State the blood parasite species.
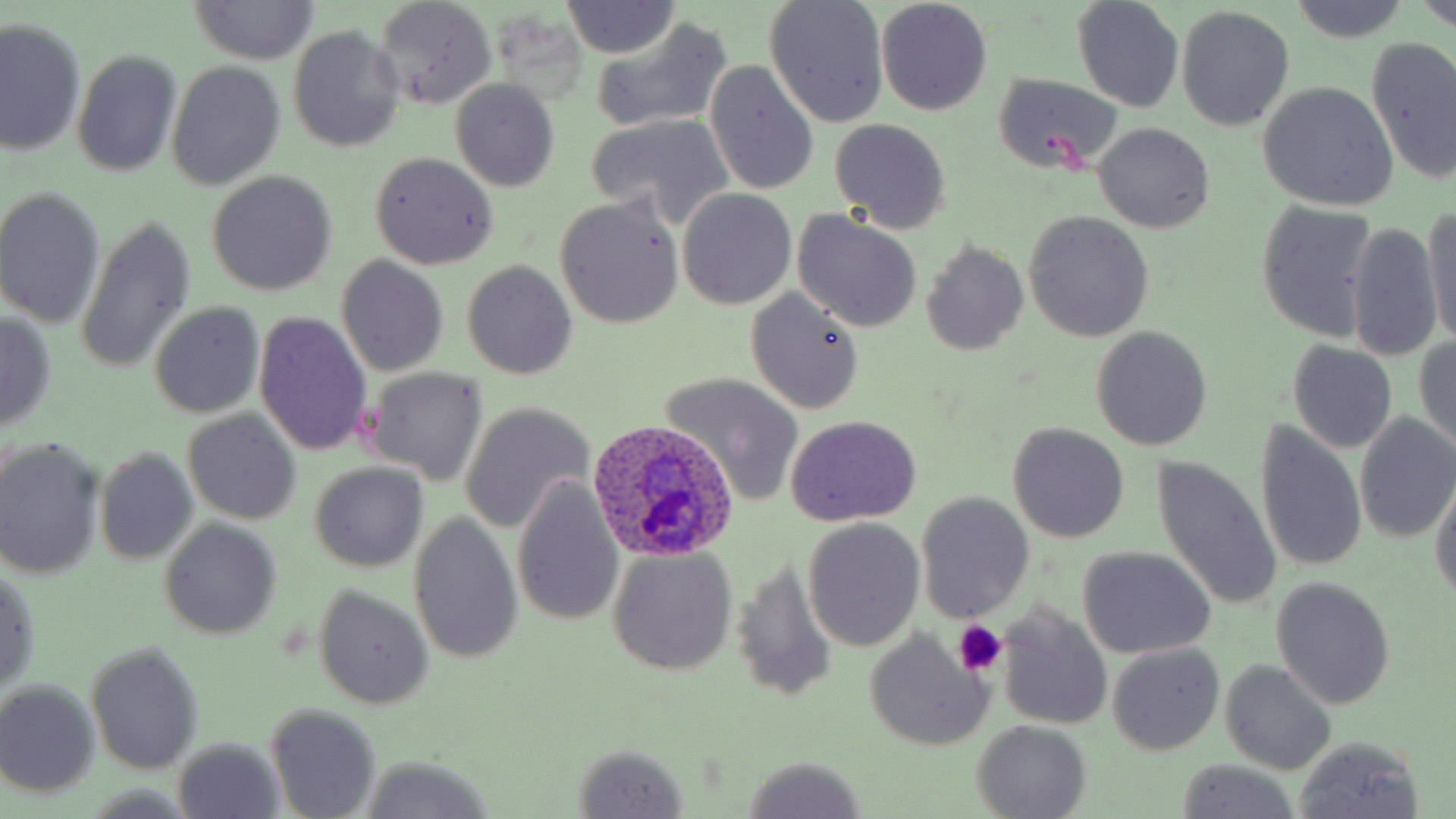
Plasmodium ovale.

Summary:
  - Coordinate format: approximate bounding boxes as (x1, y1, x2, y2) in pixels
  - Platelet locations: (951, 622, 1006, 676)
  - Uninfected red blood cell locations: (192, 0, 315, 65), (372, 0, 498, 110), (1289, 0, 1408, 42), (1420, 0, 1456, 30), (764, 1, 888, 127), (565, 2, 677, 58), (876, 2, 992, 115), (1073, 2, 1183, 113), (1177, 7, 1293, 131), (1, 18, 85, 158), (589, 18, 733, 135), (288, 25, 406, 153), (1365, 36, 1456, 187), (72, 50, 182, 177), (705, 60, 819, 196), (167, 62, 284, 188), (993, 74, 1120, 175), (450, 79, 559, 192), (1257, 82, 1397, 210), (585, 113, 735, 230), (830, 118, 952, 234), (1093, 123, 1214, 233), (370, 152, 497, 270), (208, 171, 336, 294), (0, 189, 105, 328), (678, 190, 796, 310), (555, 197, 684, 328), (1255, 203, 1378, 342), (1421, 209, 1456, 347), (793, 212, 921, 332), (1024, 212, 1154, 341), (78, 215, 194, 375), (1345, 223, 1443, 363), (921, 242, 1029, 354), (337, 256, 449, 375), (462, 261, 577, 381), (745, 290, 864, 415), (150, 302, 263, 417), (0, 310, 57, 434), (254, 311, 373, 457), (1091, 326, 1212, 451), (1414, 335, 1456, 454), (1287, 340, 1397, 454), (365, 368, 489, 484), (659, 372, 806, 506), (459, 402, 594, 533), (184, 410, 302, 526), (1354, 413, 1456, 543), (784, 415, 922, 526), (1254, 420, 1368, 576), (1006, 423, 1130, 543), (0, 440, 105, 579), (95, 448, 199, 564), (1149, 454, 1281, 615), (308, 462, 429, 573), (511, 474, 625, 629), (1430, 477, 1456, 605), (916, 492, 1035, 623), (408, 511, 522, 666), (801, 518, 925, 652), (162, 519, 280, 638), (1078, 547, 1215, 658), (606, 548, 738, 676), (731, 563, 839, 701), (0, 567, 41, 693), (1272, 577, 1395, 709), (314, 588, 432, 709), (995, 604, 1114, 730), (863, 633, 992, 750), (87, 642, 202, 774), (1108, 643, 1224, 754), (1222, 660, 1334, 774), (0, 680, 100, 799), (266, 702, 382, 818), (970, 721, 1092, 817), (1292, 734, 1425, 818), (173, 738, 283, 817), (571, 742, 689, 817), (356, 755, 492, 819), (738, 755, 869, 819), (1174, 761, 1299, 818)
  - Plasmodium ovale-infected red blood cell locations: (588, 419, 740, 562)
  - Field of view: single
  - Stain: May-Grünwald-Giemsa
  - Preparation: thin blood smear
  - Modality: light microscopy
  - Image size: 1456×819 pixels
  - Magnification: 1000x